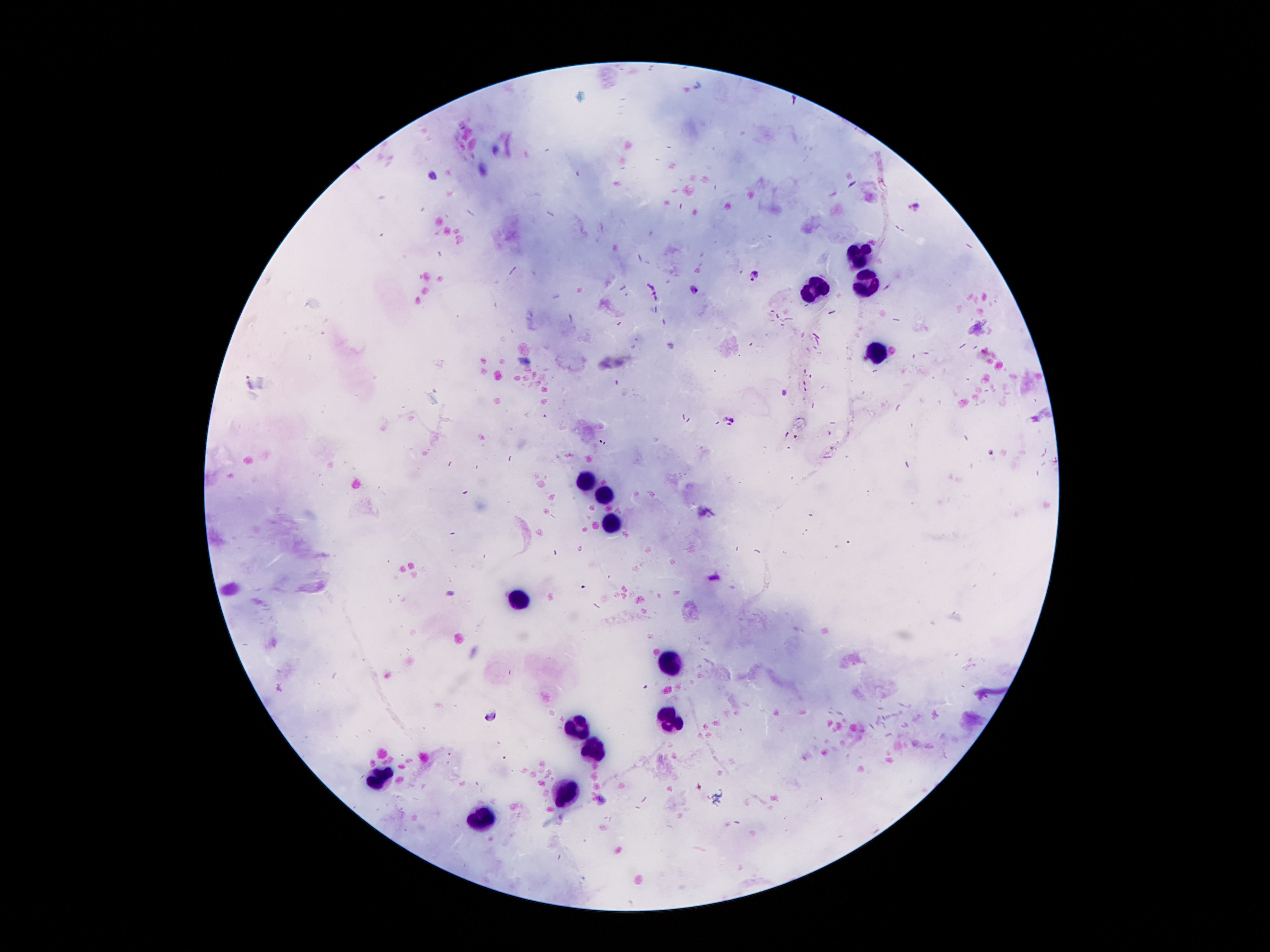
Approximate centers as (x, y) in pixels. Plasmodium parasite locations: (918, 206), (754, 274), (696, 289), (729, 421), (491, 716). Leukocyte locations: (859, 251), (866, 279), (814, 290), (874, 353), (587, 482), (606, 495), (612, 523), (520, 597), (675, 658), (669, 720), (579, 726), (597, 747), (380, 777), (565, 790), (483, 818). Image is 1270×952 pixels. Smartphone photograph taken through the microscope eyepiece. One field from this slide. Giemsa-stained preparation. Patient malaria status: infected with Plasmodium falciparum. 100x magnification. Thick blood smear.